Give a bounding box for every parasitised red blood cell, every trophozoite, every gametocyte, every leukocyte, and every artifact (platelet-like body, stain precipitate, or debris).
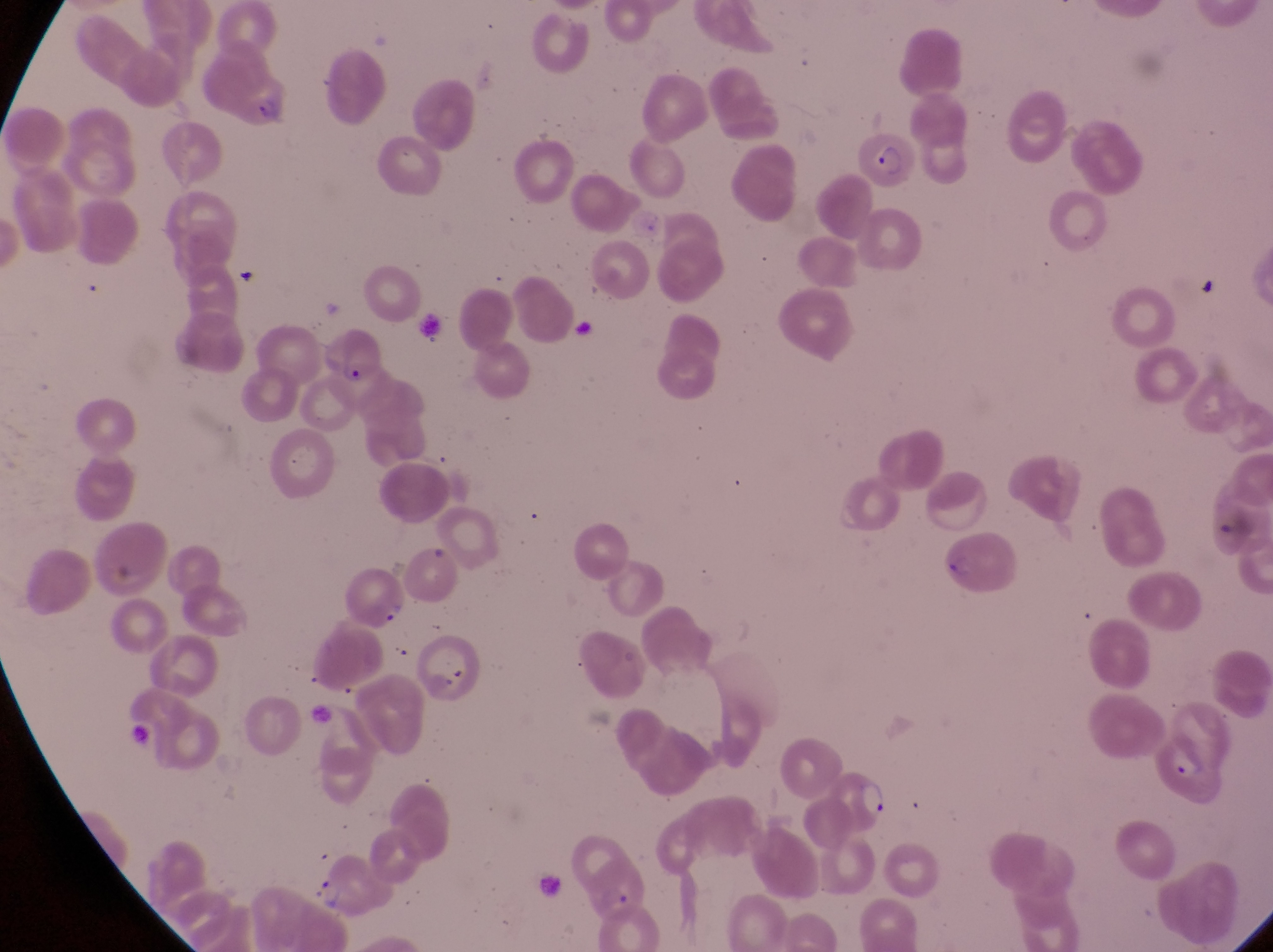

Approximate bounding boxes as left top right bottom in pixels.
Parasitised red blood cells: 856 128 914 191; 319 327 384 389; 1151 727 1234 805.
Trophozoites: 851 777 893 816; 312 871 344 913.
No leukocytes observed.
Artifacts (platelet-like body, stain precipitate, or debris): 565 318 600 345; 372 599 405 627.

Summary:
  - Field of view: single
  - Preparation: thin blood smear
  - Country: Uganda
  - Magnification: 1000x
  - Image size: 1273×952 pixels
  - Capture: smartphone photograph through the eyepiece of an Olympus CX-23 microscope